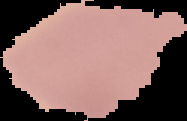

Summary:
  - Image size: 187×121 pixels
  - Preparation: thin blood film
  - Image type: cell region segmented out of the field of view; surrounding area masked to black
  - Malaria status: uninfected